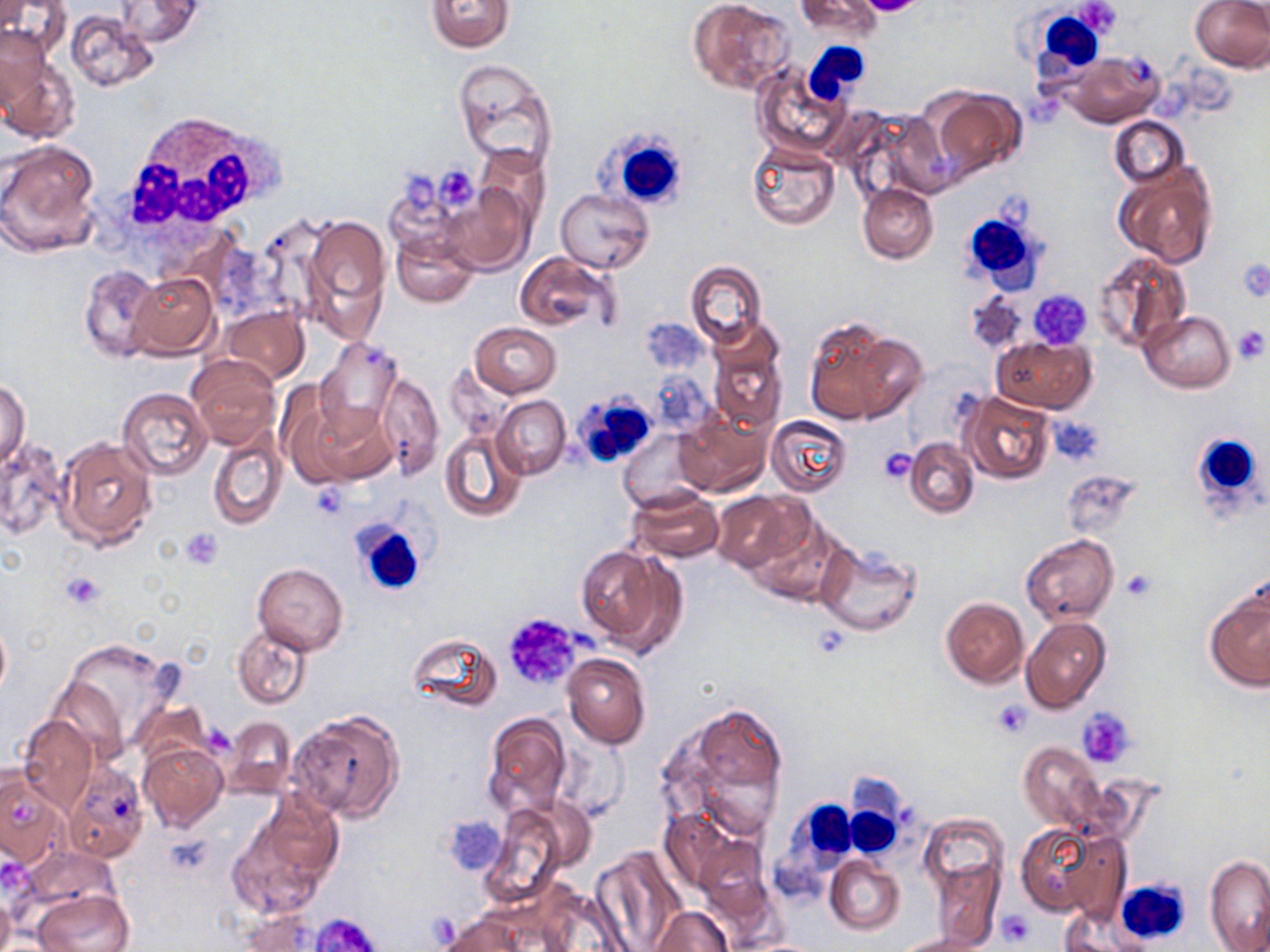 Approximate bounding boxes as (x1,y1)-(x2,y2) corner pairs in pixels. Platelet locations: (857,0)-(927,16), (1073,0)-(1123,40), (434,165)-(480,212), (403,174)-(438,213), (1235,257)-(1270,303), (1028,290)-(1093,351), (1231,325)-(1269,365), (1047,416)-(1103,464), (878,447)-(917,484), (310,481)-(352,519), (179,527)-(224,570), (1121,570)-(1156,601), (61,571)-(105,610), (501,612)-(584,693), (992,699)-(1033,736), (1077,708)-(1135,768), (445,814)-(507,877), (996,911)-(1033,947), (311,912)-(382,952). White blood cell locations: (1026,17)-(1108,76), (804,42)-(873,104), (117,113)-(282,234), (597,126)-(692,214), (958,204)-(1043,289), (570,392)-(652,462), (1187,432)-(1266,517), (351,517)-(430,599), (844,784)-(905,860), (779,796)-(861,883), (1117,879)-(1191,945). Uninfected red blood cell locations: (796,0)-(881,37), (1190,0)-(1270,72), (113,1)-(203,47), (426,1)-(514,52), (688,1)-(794,96), (65,10)-(160,93), (2,26)-(52,115), (1059,50)-(1165,129), (1,53)-(80,143), (453,60)-(558,173), (752,61)-(853,159), (925,87)-(1027,180), (1109,117)-(1188,190), (1,140)-(102,258), (747,144)-(839,230), (477,146)-(549,231), (1113,162)-(1218,269), (382,166)-(474,256), (440,182)-(532,275), (857,184)-(937,262), (556,188)-(655,273), (300,213)-(391,335), (392,233)-(477,307), (1093,249)-(1191,354), (514,251)-(615,333), (685,260)-(766,349), (78,264)-(160,363), (128,271)-(219,358), (965,290)-(1028,356), (221,306)-(309,386), (1141,311)-(1235,392), (801,317)-(921,426), (639,318)-(709,373), (470,322)-(562,398), (706,324)-(786,435), (314,337)-(402,438), (991,337)-(1095,413), (187,355)-(280,450), (376,371)-(445,480), (0,380)-(31,469), (118,387)-(212,479), (960,390)-(1057,484), (286,395)-(393,490), (492,395)-(571,480), (673,409)-(770,497), (765,415)-(854,498), (207,426)-(288,533), (439,430)-(526,523), (616,430)-(702,510), (56,435)-(157,549), (0,436)-(69,540), (905,439)-(979,518), (1060,471)-(1143,541), (627,489)-(724,562), (711,491)-(808,573), (750,512)-(848,604), (1020,533)-(1118,626), (812,542)-(921,636), (574,544)-(683,654), (251,563)-(348,654), (1205,591)-(1270,692), (940,596)-(1029,688), (0,612)-(11,703), (1021,617)-(1111,714), (232,626)-(312,708), (406,632)-(502,713), (62,640)-(179,755), (562,653)-(651,750), (45,675)-(128,762), (133,697)-(211,767), (661,700)-(792,837), (290,711)-(404,821), (483,713)-(572,817), (17,715)-(99,811), (223,717)-(297,799), (555,735)-(629,823), (138,742)-(228,832), (1019,742)-(1103,832), (62,760)-(149,862), (0,766)-(69,872), (227,801)-(340,920), (481,806)-(572,906), (660,806)-(755,893), (920,815)-(1006,893), (1016,821)-(1124,919), (590,847)-(687,951), (825,854)-(904,935), (1205,854)-(1270,950), (930,859)-(1003,949), (31,888)-(134,952), (0,892)-(14,952), (650,906)-(733,952), (1062,906)-(1151,951), (237,911)-(327,951), (440,912)-(538,952), (898,933)-(990,952). Slide-level diagnosis: negative for blood parasites. Light microscopy. Image is 1270×952 pixels. One field of a larger specimen. Thin blood smear. May-Grünwald-Giemsa stain. 1000x magnification.